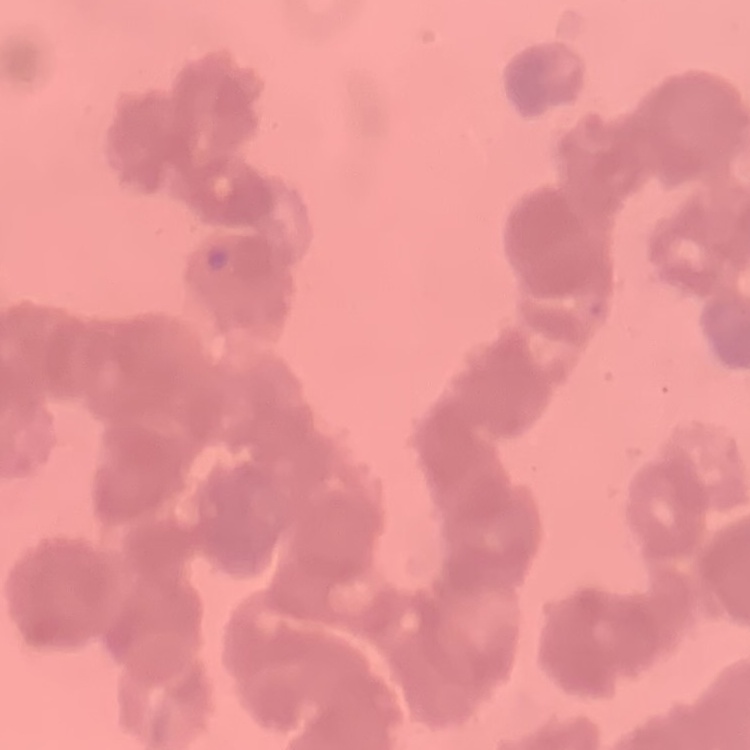 The erythrocytes exhibit rouleaux formation. Thin blood film. Field's or Giemsa stain. Square crop of a larger photomicrograph.